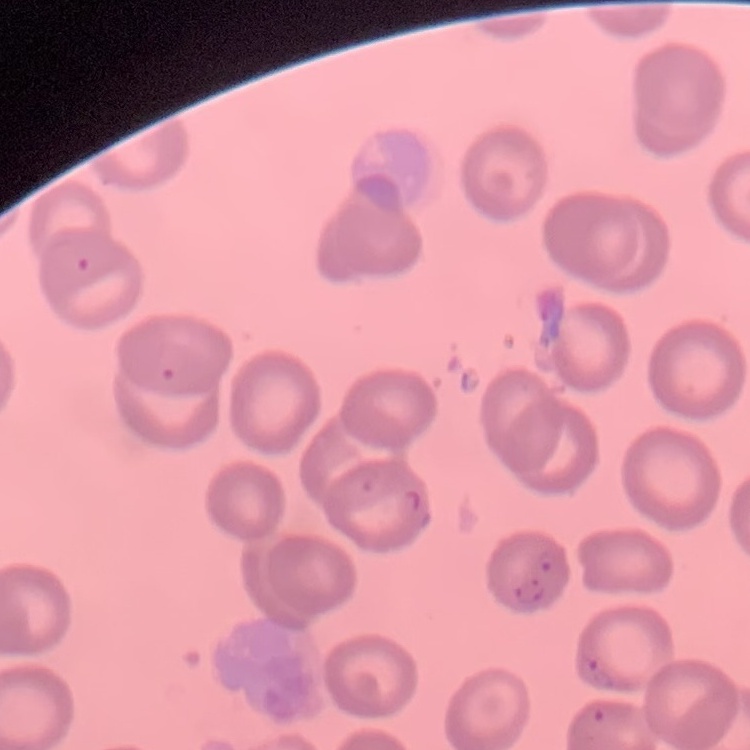 The red blood cells show no rouleaux formation. Field's or Giemsa stain. Thin blood smear. Square crop of a larger photomicrograph.